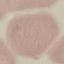

Summary:
  - Malaria status: uninfected
  - Capture: smartphone camera at the microscope eyepiece
  - Preparation: thin blood film
  - Stain: Giemsa
  - Image type: cell patch, automatically extracted from a larger field of view and resized to 64 × 64 pixels